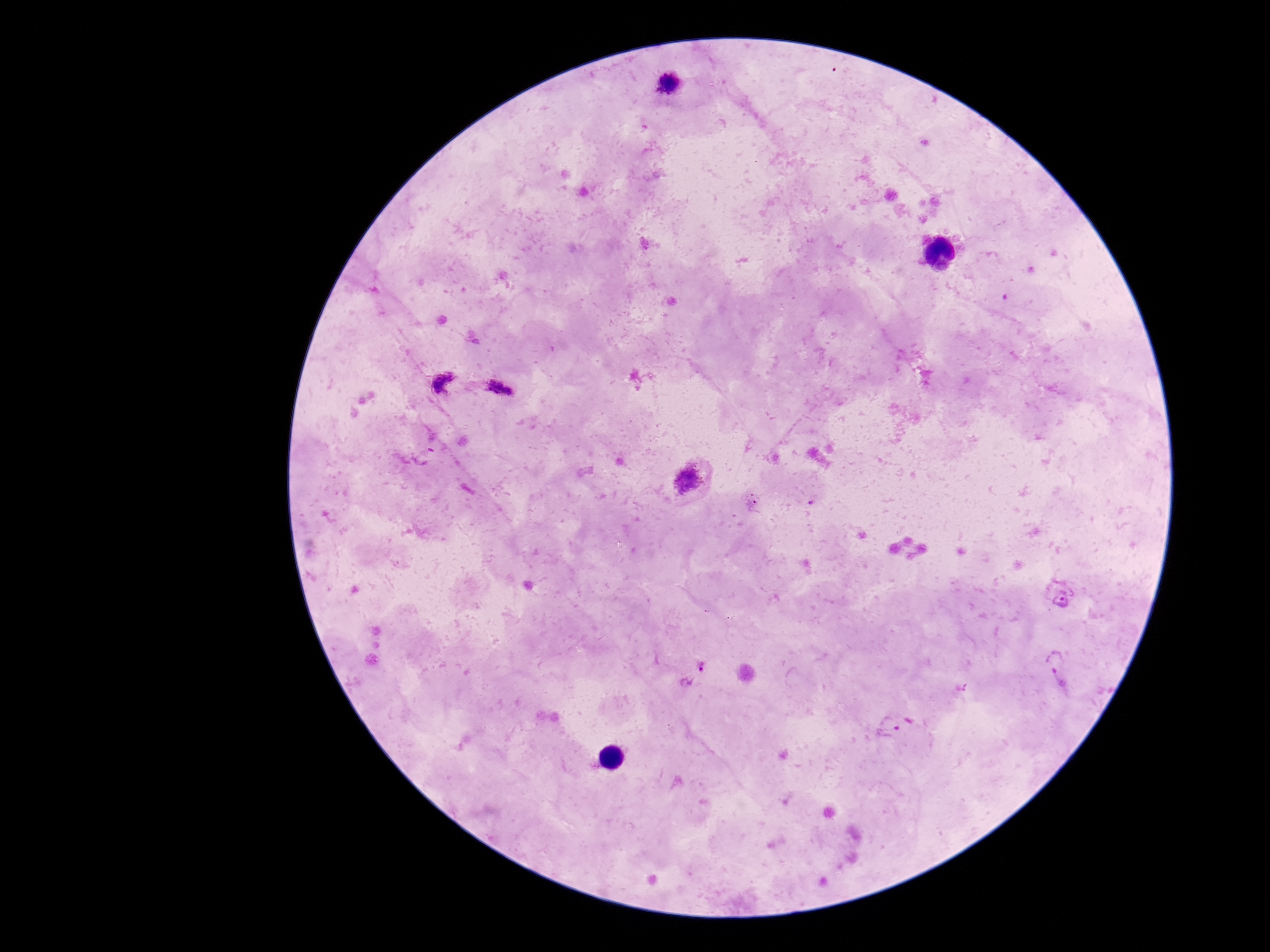
image size = 1270×952 pixels
preparation = thick peripheral-blood smear
stain = Giemsa
magnification = 100x
capture = smartphone camera through the microscope eyepiece
Plasmodium parasite locations = approximate object centers, in pixels from the top-left corner: (x=669, y=82), (x=443, y=382), (x=501, y=389), (x=687, y=479), (x=753, y=501), (x=1061, y=594), (x=1058, y=668), (x=695, y=672), (x=904, y=726)
patient malaria status = positive
field of view = single